Classify this cell by malaria status.
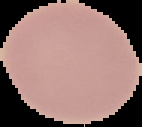

It is uninfected.

From a thin blood film. Cell region segmented out of the field of view; the surrounding area is masked to black. Image is 142×127 pixels.